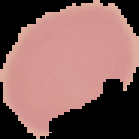
Summary:
  - Image size: 139×139 pixels
  - Preparation: thin blood smear
  - Image type: segmented cell region on a black background
  - Result: negative for malaria parasites